Locate every Plasmodium parasite.
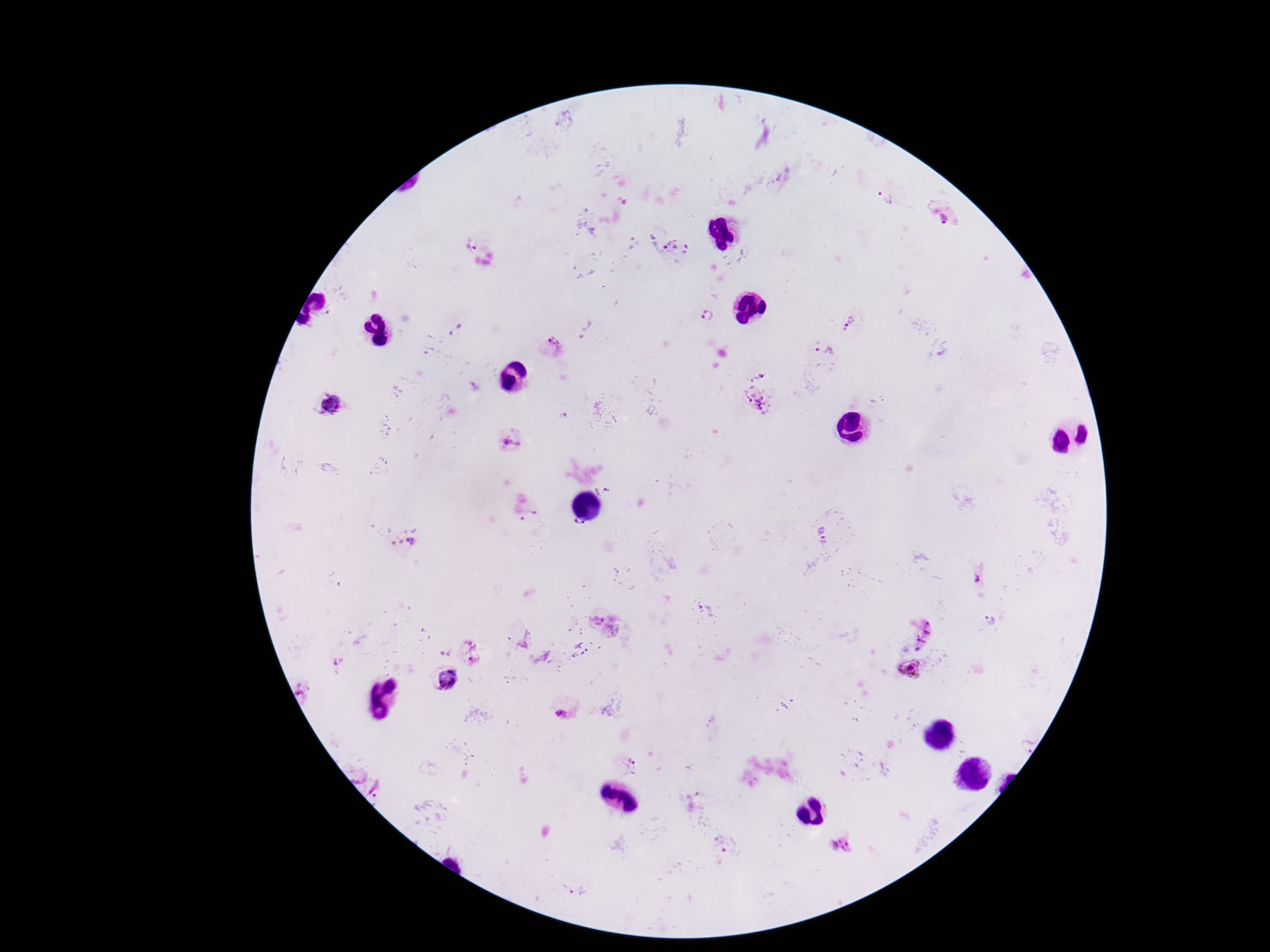

Approximate centers as [x, y] in pixels.
Plasmodium parasites: [887, 197], [947, 218], [467, 245], [672, 246], [708, 314], [850, 320], [456, 332], [552, 347], [823, 348], [759, 374], [753, 400], [328, 402], [512, 444], [604, 489], [578, 527], [822, 535], [412, 543], [978, 579], [594, 618], [992, 622], [920, 633], [467, 653], [340, 658], [910, 669], [447, 680], [305, 691], [563, 715], [1028, 745], [634, 758], [723, 843], [844, 846], [578, 891].

Image is 1270×952 pixels. Giemsa stain. Single field of view. Patient malaria status: infected. 100x magnification. Photographed through the microscope eyepiece with a smartphone camera. Thick blood film.